Assess this cell for malaria.
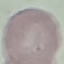
It is uninfected.

Automatically extracted cell patch, resized to 64 × 64 pixels. Acquired by smartphone through the microscope eyepiece. Giemsa-stained preparation. Thin blood smear.